Find each WBC.
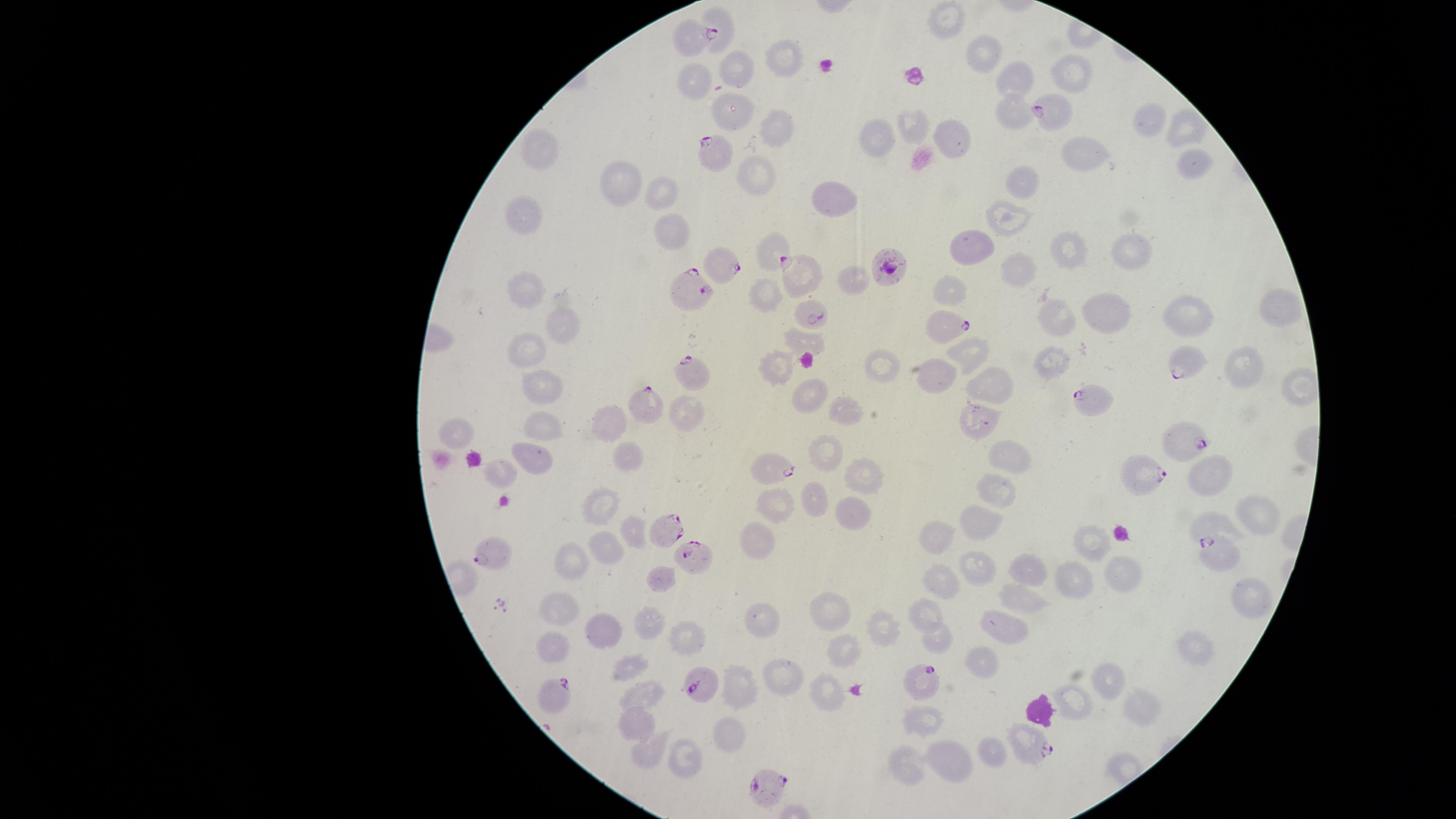
No WBCs identified.

Approximate marker points as [x, y] in pixels.
Summary:
  - Parasitized RBCs: [692, 38], [1054, 110], [714, 154], [887, 266], [726, 267], [799, 271], [693, 290], [812, 316], [946, 326], [1180, 362], [689, 370], [1092, 403], [650, 405], [1185, 437], [772, 468], [1146, 477], [667, 529], [490, 550], [1219, 552], [698, 559], [922, 679], [697, 682], [552, 695], [1027, 743], [765, 787]
  - Uninfected RBCs: [944, 15], [717, 17], [784, 57], [989, 57], [733, 71], [1069, 75], [1021, 76], [699, 79], [725, 108], [1013, 117], [1147, 117], [911, 122], [777, 129], [1185, 129], [950, 135], [878, 137], [539, 144], [1082, 151], [1194, 159], [752, 179], [628, 182], [1027, 183], [660, 191], [841, 192], [1013, 217], [525, 218], [671, 232], [981, 242], [769, 244], [1063, 246], [1123, 248], [1012, 266], [848, 277], [768, 290], [528, 291], [945, 291], [1274, 308], [1109, 316], [1186, 317], [1051, 320], [559, 329], [799, 340], [526, 345], [964, 353], [1054, 363], [883, 364], [1241, 367], [775, 371], [931, 380], [542, 381], [997, 390], [1298, 391], [807, 397], [843, 412], [682, 413], [607, 416], [983, 424], [542, 427], [456, 433], [823, 449], [627, 458], [1008, 460], [526, 462], [1212, 471], [492, 476], [861, 477], [995, 492], [814, 500], [773, 504], [855, 508], [597, 511], [1254, 512], [985, 517], [1215, 523], [937, 534], [630, 536], [758, 540], [608, 548], [1093, 548], [572, 562], [980, 564], [1039, 565], [1126, 570], [660, 577], [941, 579], [1072, 584], [1250, 596], [1027, 597], [555, 608], [831, 608], [926, 610], [764, 618], [649, 628], [1003, 628], [610, 631], [886, 632], [688, 635], [935, 638], [843, 640], [1194, 647], [548, 649], [982, 660], [634, 663], [787, 670], [740, 682], [1103, 685], [648, 686], [821, 693], [1068, 704], [1131, 709], [932, 719], [639, 727], [723, 734], [991, 751], [684, 753], [647, 757], [955, 761], [903, 767]
  - Stain: Giemsa
  - Visible region: circular
  - Field of view: single
  - Preparation: thin smear of blood
  - Capture: smartphone photograph through the microscope eyepiece
  - Species: Plasmodium falciparum
  - Image size: 1456×819 pixels
  - Presence: malaria parasites identified